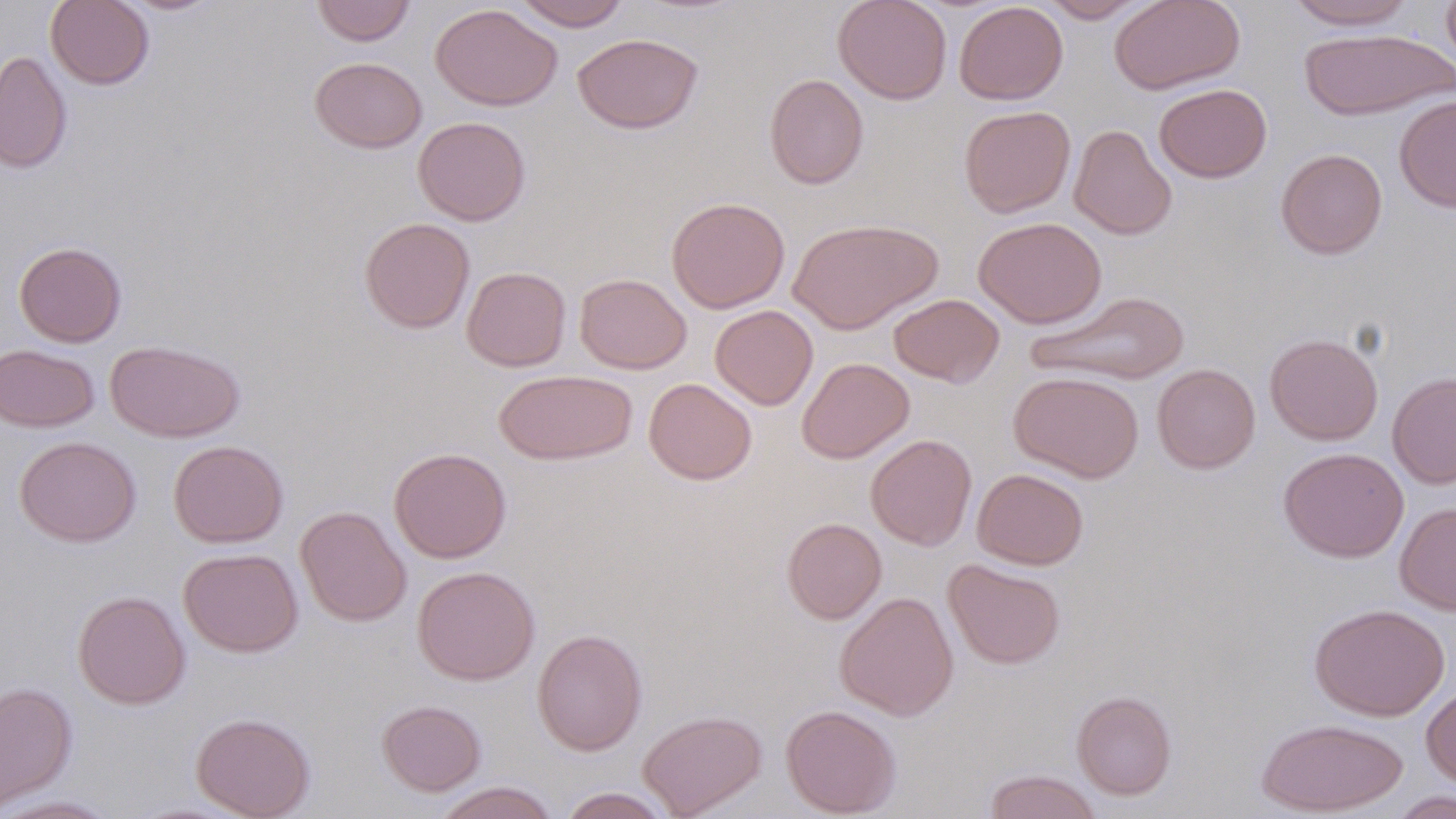

slide-level diagnosis = no evidence of blood parasites
preparation = thin blood film
modality = optical microscopy
magnification = 1000x
uninfected red blood cell locations = approximate bounding boxes as named x1/y1/x2/y2 corners in pixels: (x1=45, y1=0, x2=155, y2=90), (x1=118, y1=0, x2=224, y2=15), (x1=311, y1=0, x2=415, y2=46), (x1=512, y1=0, x2=632, y2=31), (x1=833, y1=0, x2=952, y2=105), (x1=1039, y1=0, x2=1150, y2=23), (x1=1109, y1=0, x2=1245, y2=95), (x1=1284, y1=0, x2=1419, y2=30), (x1=1441, y1=0, x2=1456, y2=78), (x1=954, y1=1, x2=1068, y2=105), (x1=430, y1=3, x2=562, y2=111), (x1=1299, y1=29, x2=1454, y2=122), (x1=572, y1=33, x2=703, y2=134), (x1=0, y1=50, x2=73, y2=173), (x1=309, y1=56, x2=427, y2=153), (x1=764, y1=73, x2=869, y2=189), (x1=1154, y1=83, x2=1272, y2=183), (x1=1394, y1=95, x2=1456, y2=212), (x1=958, y1=105, x2=1076, y2=218), (x1=413, y1=116, x2=531, y2=225), (x1=1069, y1=124, x2=1177, y2=241), (x1=1275, y1=149, x2=1388, y2=260), (x1=666, y1=196, x2=790, y2=313), (x1=973, y1=216, x2=1106, y2=329), (x1=359, y1=217, x2=475, y2=333), (x1=788, y1=217, x2=943, y2=335), (x1=14, y1=241, x2=127, y2=347), (x1=462, y1=266, x2=571, y2=371), (x1=574, y1=273, x2=691, y2=374), (x1=1025, y1=289, x2=1192, y2=387), (x1=888, y1=294, x2=1005, y2=388), (x1=710, y1=305, x2=818, y2=410), (x1=1264, y1=333, x2=1383, y2=445), (x1=106, y1=340, x2=245, y2=442), (x1=0, y1=344, x2=99, y2=432), (x1=797, y1=357, x2=914, y2=462), (x1=1152, y1=363, x2=1261, y2=474), (x1=493, y1=370, x2=637, y2=465), (x1=1008, y1=370, x2=1144, y2=482), (x1=1387, y1=371, x2=1456, y2=489), (x1=643, y1=378, x2=757, y2=485), (x1=865, y1=433, x2=977, y2=551), (x1=14, y1=435, x2=141, y2=547), (x1=168, y1=440, x2=288, y2=547), (x1=389, y1=447, x2=512, y2=563), (x1=1278, y1=447, x2=1409, y2=563), (x1=972, y1=468, x2=1088, y2=570), (x1=1394, y1=501, x2=1456, y2=615), (x1=295, y1=505, x2=412, y2=626), (x1=782, y1=517, x2=887, y2=623), (x1=178, y1=548, x2=303, y2=657), (x1=943, y1=559, x2=1065, y2=670), (x1=412, y1=566, x2=540, y2=685), (x1=72, y1=590, x2=190, y2=709), (x1=835, y1=591, x2=959, y2=721), (x1=1310, y1=602, x2=1450, y2=721), (x1=532, y1=628, x2=648, y2=756), (x1=0, y1=681, x2=77, y2=812), (x1=1421, y1=683, x2=1456, y2=791), (x1=1072, y1=690, x2=1176, y2=799), (x1=377, y1=700, x2=486, y2=796), (x1=780, y1=703, x2=902, y2=817), (x1=637, y1=709, x2=768, y2=818), (x1=191, y1=712, x2=316, y2=819), (x1=1255, y1=717, x2=1409, y2=816), (x1=983, y1=769, x2=1102, y2=819), (x1=430, y1=781, x2=560, y2=819), (x1=558, y1=787, x2=674, y2=818), (x1=1387, y1=790, x2=1455, y2=818), (x1=0, y1=795, x2=123, y2=818)
stain = May-Grünwald-Giemsa
field of view = single
image size = 1456×819 pixels